Classify this cell by malaria status.
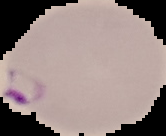

It is parasitized.

Summary:
  - Preparation: thin blood film
  - Image size: 166×136 pixels
  - Image type: segmented cell region with the area outside set to black